Assess this cell for malaria.
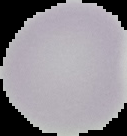

It is uninfected.

Image is 127×136 pixels. From a thin blood film. Segmented cell region on a black background.